Locate every Plasmodium parasite.
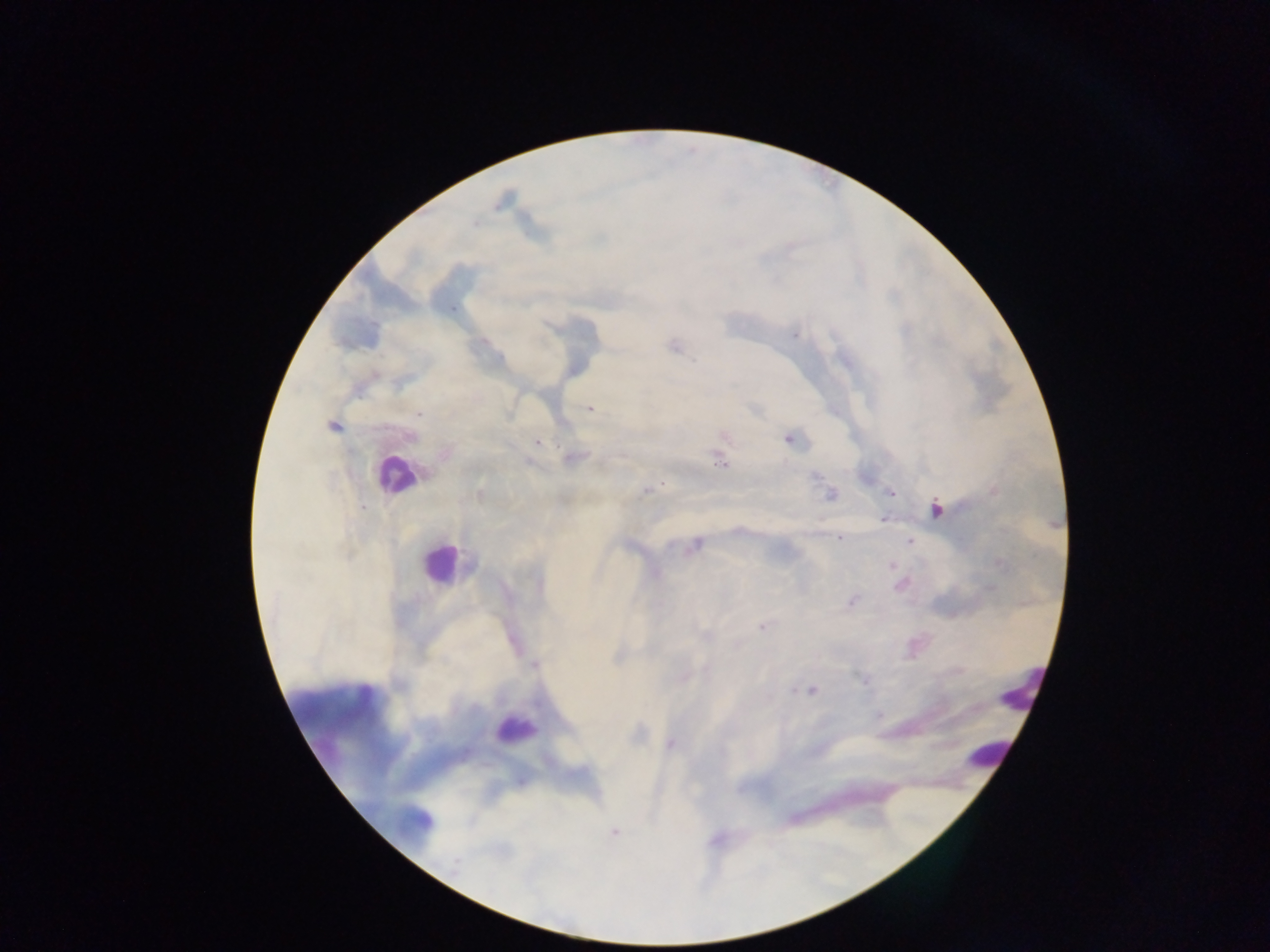
Approximate centers as {x, y} in pixels.
Plasmodium parasites: {795, 335}, {675, 346}, {592, 409}, {419, 414}, {332, 426}, {789, 439}, {537, 442}, {572, 458}, {720, 463}, {816, 476}, {646, 490}, {890, 493}, {830, 495}, {362, 507}, {936, 510}, {883, 519}, {839, 538}, {910, 541}, {697, 545}, {891, 565}, {851, 601}, {762, 627}, {700, 636}, {535, 665}, {707, 668}, {864, 680}, {793, 690}, {812, 690}, {670, 745}, {615, 833}, {456, 864}.

Summary:
  - Leukocyte locations: {394, 474}, {438, 564}, {1012, 695}, {513, 732}, {979, 757}
  - Image size: 1270×952 pixels
  - Capture: mobile-phone photograph through a microscope
  - Field of view: single
  - Country: Ghana
  - Preparation: thick blood smear